Point out every malaria parasite.
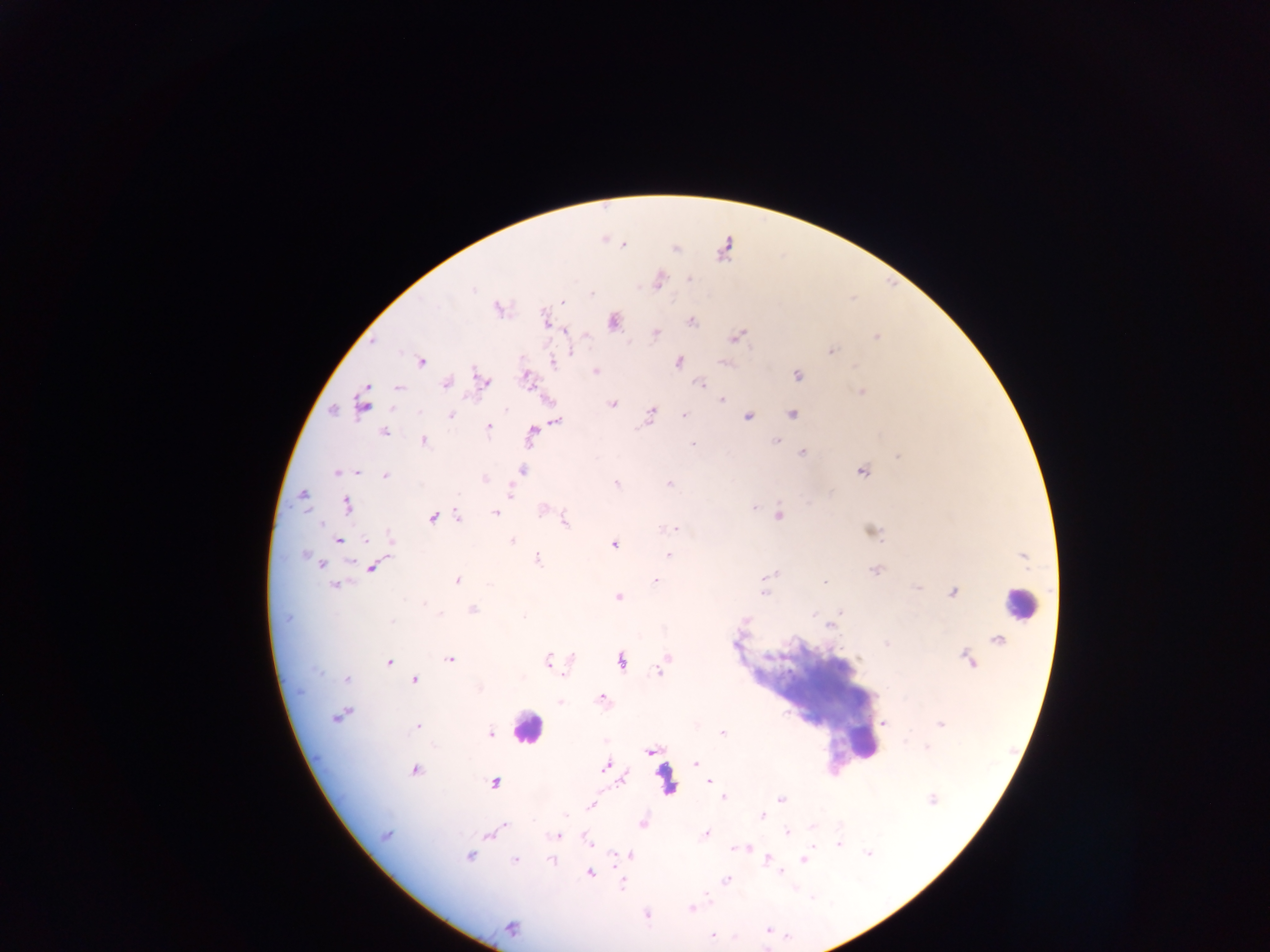

Approximate centers as (x, y) in pixels.
Malaria parasites: (623, 245), (676, 248), (658, 281), (562, 302), (498, 308), (613, 320), (690, 320), (545, 321), (566, 331), (656, 333), (737, 336), (876, 337), (831, 351), (420, 361), (552, 361), (677, 361), (726, 362), (596, 371), (797, 376), (526, 379), (483, 380), (445, 383), (699, 383), (398, 387), (861, 391), (722, 400), (363, 403), (613, 404), (333, 410), (792, 414), (450, 415), (650, 415), (748, 415), (684, 416), (555, 420), (488, 426), (384, 431), (532, 431), (423, 440), (776, 440), (802, 453), (899, 455), (522, 470), (861, 470), (338, 471), (357, 471), (386, 476), (485, 478), (615, 483), (669, 483), (509, 491), (301, 495), (347, 505), (754, 506), (496, 512), (778, 514), (458, 515), (433, 517), (563, 521), (674, 527), (666, 529), (871, 531), (337, 540), (390, 541), (511, 541), (614, 543), (668, 554), (537, 559), (320, 564), (371, 566), (876, 569), (455, 581), (655, 581), (824, 583), (335, 584), (952, 591), (763, 592), (618, 597), (471, 610), (523, 615), (831, 624), (999, 639), (666, 658), (450, 659), (548, 660), (621, 660), (969, 660), (388, 662), (660, 668), (345, 678), (414, 680), (601, 698), (560, 702), (340, 714), (884, 723), (941, 723), (416, 725), (722, 733), (490, 734), (650, 752), (695, 763), (605, 766), (415, 770), (621, 779), (709, 781), (493, 783), (724, 797), (780, 798), (931, 799), (590, 804), (762, 815), (642, 823), (504, 825), (787, 833), (385, 834), (488, 834), (706, 834), (558, 835), (586, 837), (837, 844), (747, 848), (868, 852), (630, 854), (469, 855), (767, 859), (803, 859), (515, 860), (552, 860), (589, 872), (622, 880), (725, 880), (692, 908), (645, 914), (511, 927), (713, 934).

preparation: thick blood film
image_size: 1270×952 pixels
country: Ghana
leukocyte_locations: 'approximate centers as (x, y) in pixels: (1020, 604), (815, 696), (528, 728), (865, 744), (666, 782)'
field_of_view: single
capture: mobile-phone photograph through a microscope